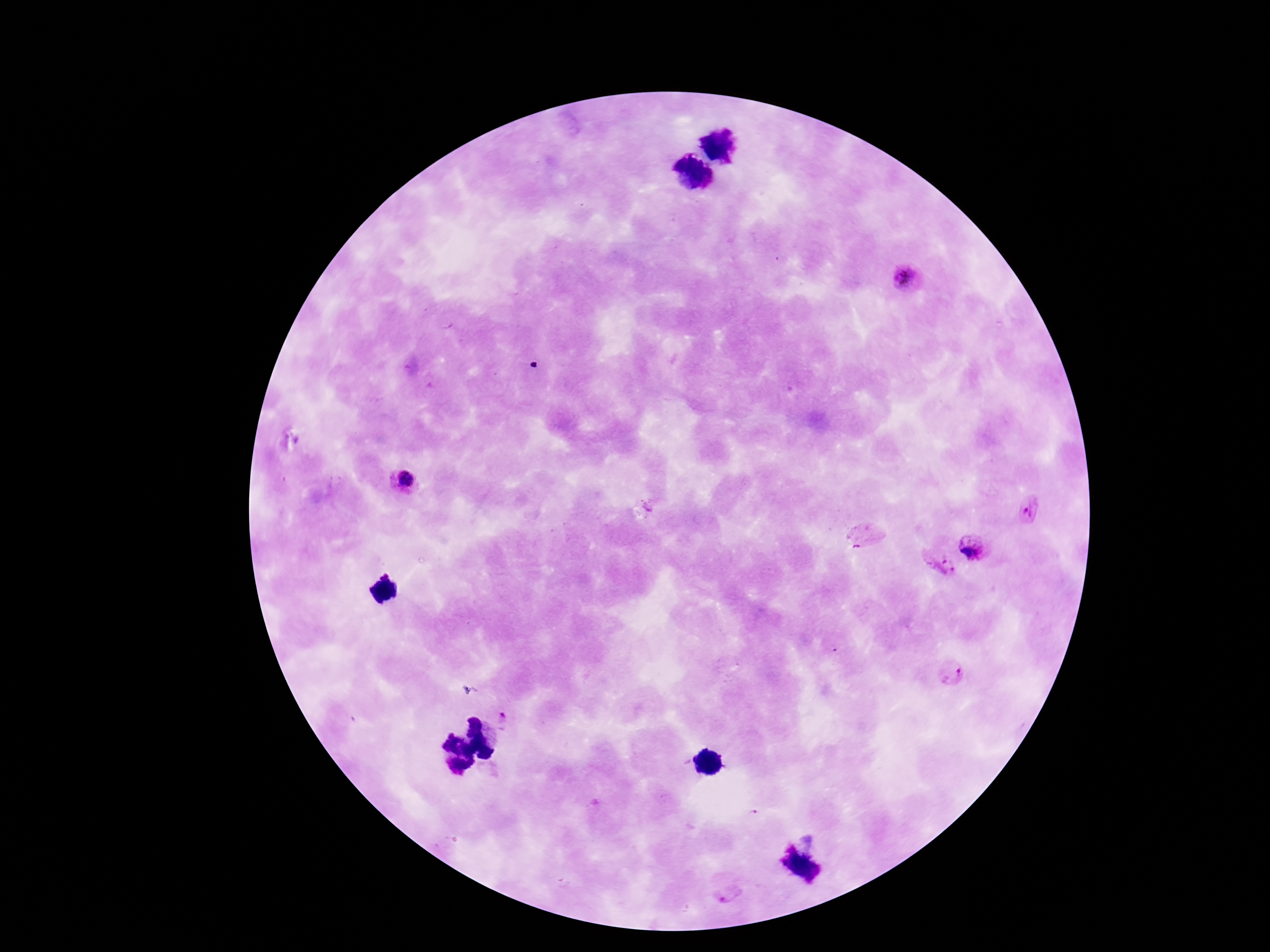
Approximate centers as {x, y} in pixels.
Summary:
  - Plasmodium parasite locations: {906, 278}, {405, 480}, {1030, 507}, {862, 539}, {974, 547}, {939, 564}, {951, 671}, {506, 717}, {728, 897}
  - Preparation: thick blood smear
  - Capture: smartphone camera through the microscope eyepiece
  - Field of view: single
  - Image size: 1270×952 pixels
  - Stain: Giemsa
  - Patient malaria status: infected
  - Magnification: 100x